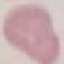

result: no malaria parasites seen
image_type: cell patch, automatically extracted from a larger field of view and resized to 64 × 64 pixels
preparation: thin smear
stain: Giemsa
capture: smartphone camera at the microscope eyepiece